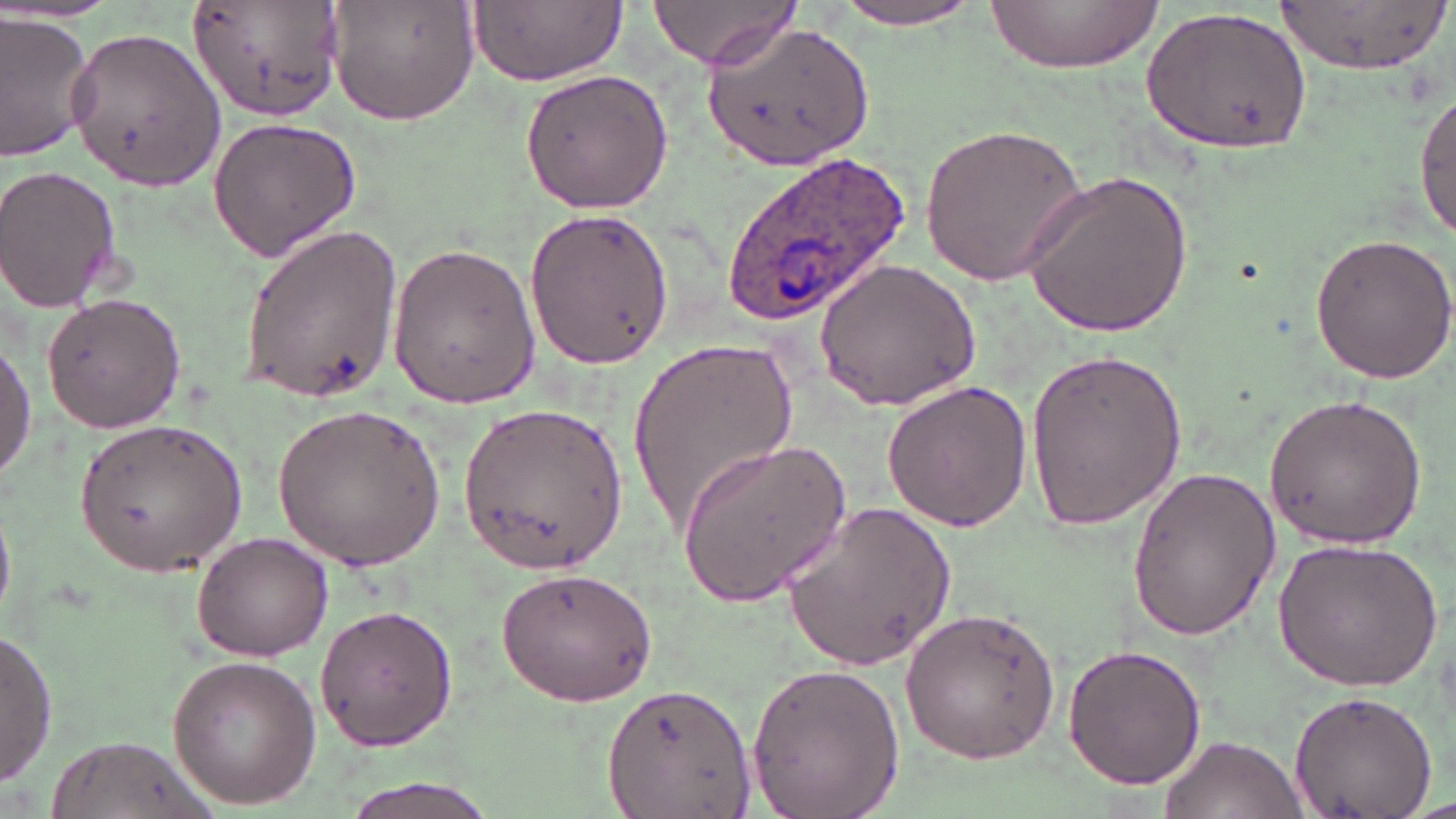

Approximate bounding boxes as named x1/y1/x2/y2 corners in pixels. Uninfected red blood cell locations: (x1=188, y1=0, x2=344, y2=122), (x1=327, y1=0, x2=478, y2=125), (x1=464, y1=0, x2=627, y2=89), (x1=822, y1=0, x2=992, y2=29), (x1=1274, y1=0, x2=1452, y2=72), (x1=644, y1=1, x2=798, y2=71), (x1=987, y1=2, x2=1163, y2=74), (x1=1141, y1=5, x2=1313, y2=157), (x1=2, y1=15, x2=97, y2=160), (x1=706, y1=19, x2=873, y2=170), (x1=67, y1=26, x2=225, y2=192), (x1=520, y1=67, x2=673, y2=214), (x1=1414, y1=85, x2=1455, y2=242), (x1=207, y1=117, x2=360, y2=261), (x1=919, y1=119, x2=1092, y2=285), (x1=0, y1=165, x2=125, y2=311), (x1=1022, y1=169, x2=1196, y2=338), (x1=524, y1=210, x2=672, y2=368), (x1=240, y1=222, x2=404, y2=404), (x1=1306, y1=230, x2=1456, y2=385), (x1=386, y1=245, x2=542, y2=407), (x1=814, y1=258, x2=982, y2=412), (x1=41, y1=289, x2=186, y2=432), (x1=0, y1=336, x2=35, y2=486), (x1=629, y1=336, x2=795, y2=537), (x1=1023, y1=345, x2=1187, y2=530), (x1=880, y1=380, x2=1032, y2=530), (x1=1263, y1=391, x2=1427, y2=552), (x1=459, y1=400, x2=629, y2=572), (x1=271, y1=403, x2=448, y2=571), (x1=76, y1=419, x2=247, y2=574), (x1=676, y1=436, x2=853, y2=606), (x1=1125, y1=464, x2=1282, y2=642), (x1=0, y1=500, x2=13, y2=626), (x1=780, y1=500, x2=960, y2=670), (x1=192, y1=532, x2=333, y2=660), (x1=1273, y1=536, x2=1443, y2=692), (x1=496, y1=566, x2=655, y2=706), (x1=315, y1=603, x2=458, y2=752), (x1=901, y1=604, x2=1061, y2=767), (x1=0, y1=629, x2=57, y2=785), (x1=1062, y1=646, x2=1208, y2=789), (x1=162, y1=654, x2=322, y2=807), (x1=745, y1=660, x2=906, y2=819), (x1=604, y1=681, x2=756, y2=819), (x1=1285, y1=688, x2=1436, y2=817), (x1=1159, y1=732, x2=1307, y2=819), (x1=51, y1=735, x2=211, y2=819), (x1=344, y1=778, x2=499, y2=819). Plasmodium ovale-infected red blood cell locations: (x1=719, y1=150, x2=911, y2=331). Slide-level diagnosis: Plasmodium ovale. Image is 1456×819 pixels. Captured at 1000x magnification. Light microscopy. Thin blood film. One field of a larger specimen. May-Grünwald-Giemsa stain.